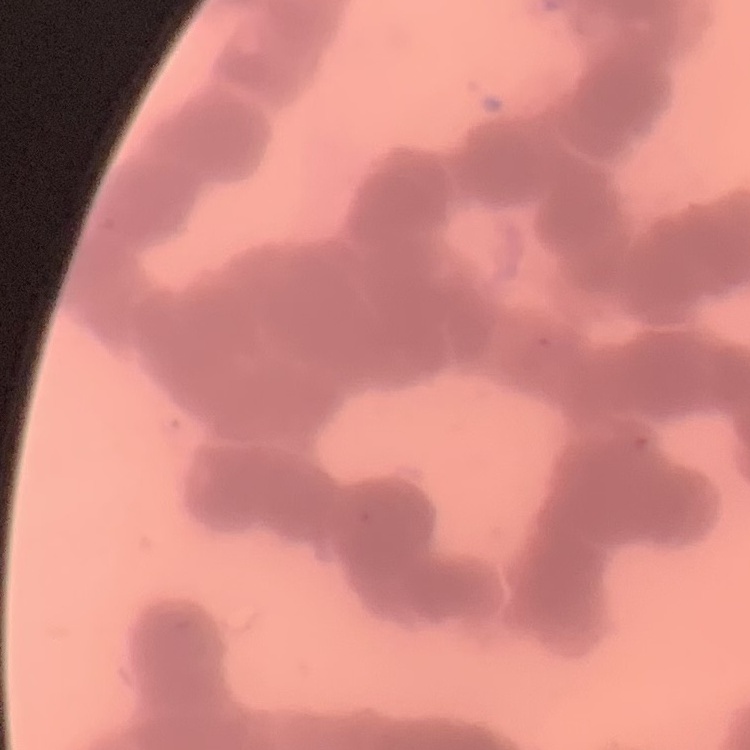

erythrocyte morphology = rouleaux formation
stain = Field's or Giemsa
image type = one tile cut from a larger photomicrograph
preparation = thin blood film